Name the blood parasite species.
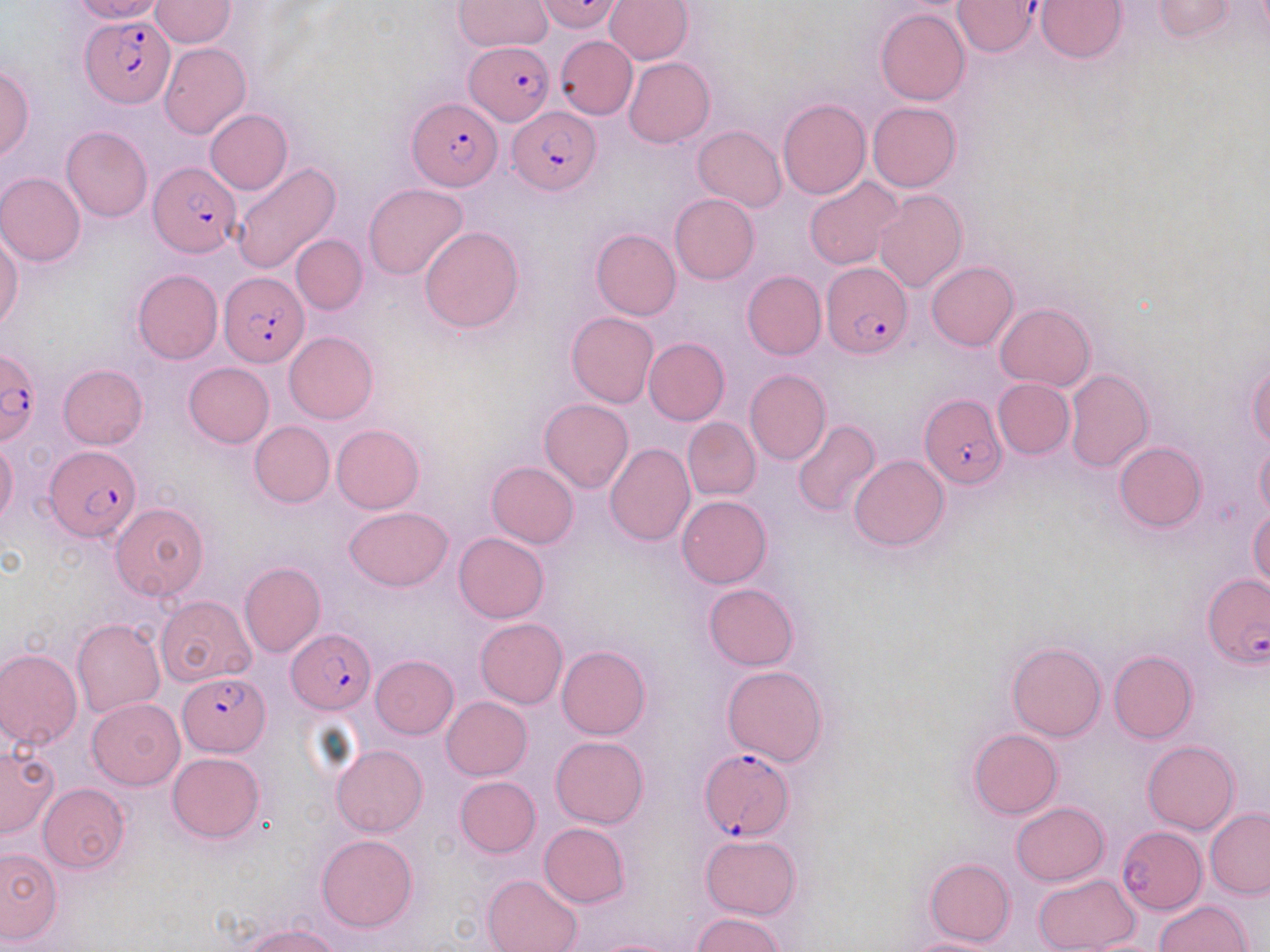

Plasmodium falciparum.

Summary:
  - Coordinate format: approximate bounding boxes as named x1/y1/x2/y2 corners in pixels
  - Uninfected red blood cell locations (subset): (x1=72, y1=0, x2=166, y2=23), (x1=150, y1=0, x2=237, y2=47), (x1=537, y1=0, x2=625, y2=33), (x1=605, y1=0, x2=693, y2=63), (x1=1037, y1=0, x2=1126, y2=62), (x1=1152, y1=0, x2=1236, y2=40), (x1=453, y1=1, x2=554, y2=52), (x1=876, y1=9, x2=970, y2=105), (x1=555, y1=35, x2=638, y2=119), (x1=158, y1=43, x2=251, y2=139), (x1=624, y1=56, x2=714, y2=148), (x1=0, y1=64, x2=34, y2=161), (x1=778, y1=99, x2=871, y2=200), (x1=868, y1=102, x2=961, y2=192), (x1=205, y1=109, x2=292, y2=194), (x1=62, y1=126, x2=152, y2=222), (x1=693, y1=126, x2=786, y2=211), (x1=230, y1=161, x2=342, y2=274), (x1=1, y1=173, x2=85, y2=266), (x1=803, y1=177, x2=905, y2=271), (x1=364, y1=184, x2=469, y2=280), (x1=873, y1=190, x2=967, y2=292), (x1=670, y1=194, x2=759, y2=283), (x1=420, y1=226, x2=523, y2=333), (x1=591, y1=229, x2=681, y2=320), (x1=0, y1=232, x2=22, y2=331), (x1=291, y1=234, x2=367, y2=314), (x1=926, y1=262, x2=1019, y2=350), (x1=132, y1=269, x2=223, y2=364), (x1=741, y1=270, x2=826, y2=360), (x1=994, y1=302, x2=1094, y2=390), (x1=567, y1=312, x2=658, y2=408), (x1=284, y1=331, x2=378, y2=424), (x1=644, y1=337, x2=729, y2=426), (x1=184, y1=363, x2=274, y2=448), (x1=1246, y1=363, x2=1270, y2=448), (x1=58, y1=364, x2=147, y2=449), (x1=1064, y1=367, x2=1153, y2=473), (x1=745, y1=369, x2=831, y2=466), (x1=993, y1=378, x2=1075, y2=458), (x1=539, y1=398, x2=633, y2=492), (x1=682, y1=416, x2=760, y2=500), (x1=791, y1=420, x2=881, y2=518), (x1=249, y1=421, x2=334, y2=507), (x1=331, y1=425, x2=424, y2=514), (x1=0, y1=439, x2=18, y2=524), (x1=1114, y1=442, x2=1206, y2=533), (x1=605, y1=443, x2=695, y2=546), (x1=1256, y1=443, x2=1270, y2=521), (x1=849, y1=455, x2=948, y2=550), (x1=486, y1=461, x2=578, y2=548), (x1=677, y1=495, x2=772, y2=589), (x1=110, y1=502, x2=209, y2=600), (x1=1248, y1=506, x2=1270, y2=593), (x1=344, y1=507, x2=453, y2=591), (x1=454, y1=532, x2=549, y2=623), (x1=239, y1=562, x2=325, y2=656), (x1=702, y1=584, x2=799, y2=671), (x1=155, y1=595, x2=256, y2=686), (x1=474, y1=618, x2=567, y2=708), (x1=72, y1=619, x2=165, y2=718), (x1=1007, y1=641, x2=1106, y2=741), (x1=558, y1=646, x2=650, y2=740), (x1=0, y1=648, x2=82, y2=751), (x1=1109, y1=649, x2=1197, y2=743), (x1=371, y1=655, x2=459, y2=739), (x1=722, y1=665, x2=828, y2=766), (x1=87, y1=697, x2=185, y2=789), (x1=442, y1=697, x2=532, y2=780), (x1=968, y1=728, x2=1062, y2=819), (x1=551, y1=736, x2=648, y2=828), (x1=1142, y1=741, x2=1240, y2=835), (x1=331, y1=744, x2=426, y2=837), (x1=0, y1=745, x2=59, y2=837), (x1=168, y1=753, x2=265, y2=843), (x1=454, y1=776, x2=540, y2=858), (x1=39, y1=783, x2=130, y2=873), (x1=1010, y1=803, x2=1109, y2=885), (x1=1205, y1=808, x2=1270, y2=898), (x1=539, y1=822, x2=629, y2=908), (x1=1116, y1=825, x2=1206, y2=914), (x1=700, y1=834, x2=801, y2=919), (x1=316, y1=835, x2=418, y2=932), (x1=0, y1=848, x2=62, y2=945), (x1=925, y1=857, x2=1015, y2=947), (x1=483, y1=873, x2=583, y2=952), (x1=1031, y1=873, x2=1141, y2=952), (x1=1155, y1=900, x2=1252, y2=951), (x1=691, y1=912, x2=787, y2=952), (x1=245, y1=924, x2=341, y2=951), (x1=591, y1=937, x2=687, y2=952), (x1=902, y1=937, x2=1009, y2=952)
  - Plasmodium falciparum-infected red blood cell locations (subset): (x1=83, y1=15, x2=174, y2=106), (x1=465, y1=42, x2=555, y2=124), (x1=408, y1=97, x2=503, y2=190), (x1=508, y1=105, x2=599, y2=194), (x1=149, y1=162, x2=240, y2=257), (x1=823, y1=261, x2=912, y2=359), (x1=218, y1=272, x2=310, y2=367), (x1=0, y1=349, x2=41, y2=446), (x1=918, y1=392, x2=1005, y2=489), (x1=43, y1=447, x2=140, y2=541), (x1=1203, y1=573, x2=1268, y2=669), (x1=288, y1=629, x2=375, y2=714), (x1=178, y1=671, x2=270, y2=756), (x1=698, y1=747, x2=792, y2=840)
  - Field of view: single
  - Image size: 1270×952 pixels
  - Preparation: thin blood smear
  - Magnification: 1000x
  - Modality: light microscopy
  - Stain: May-Grünwald-Giemsa